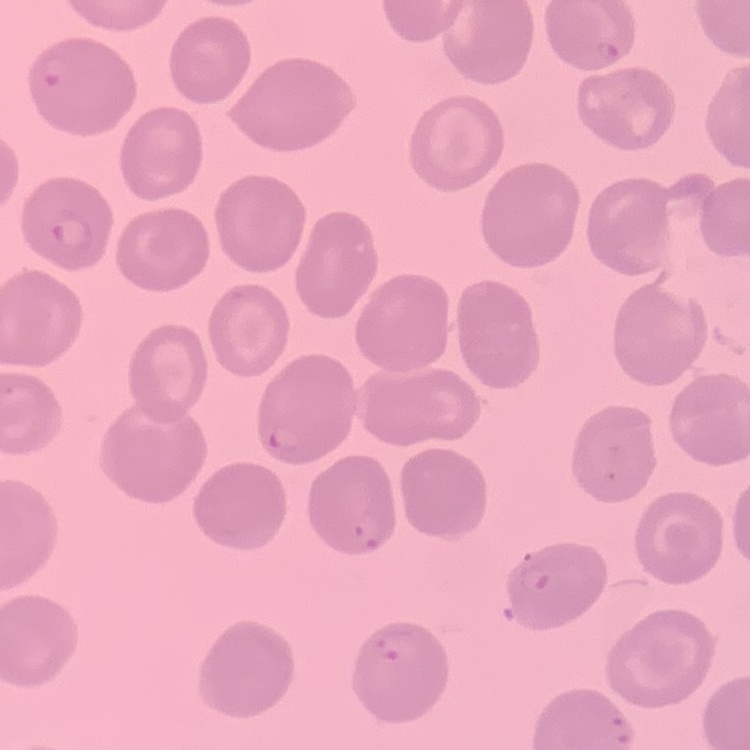
Summary:
  - Red blood cell morphology: no rouleaux formation
  - Preparation: thin blood film
  - Stain: Field's or Giemsa
  - Image type: square crop of a larger photomicrograph